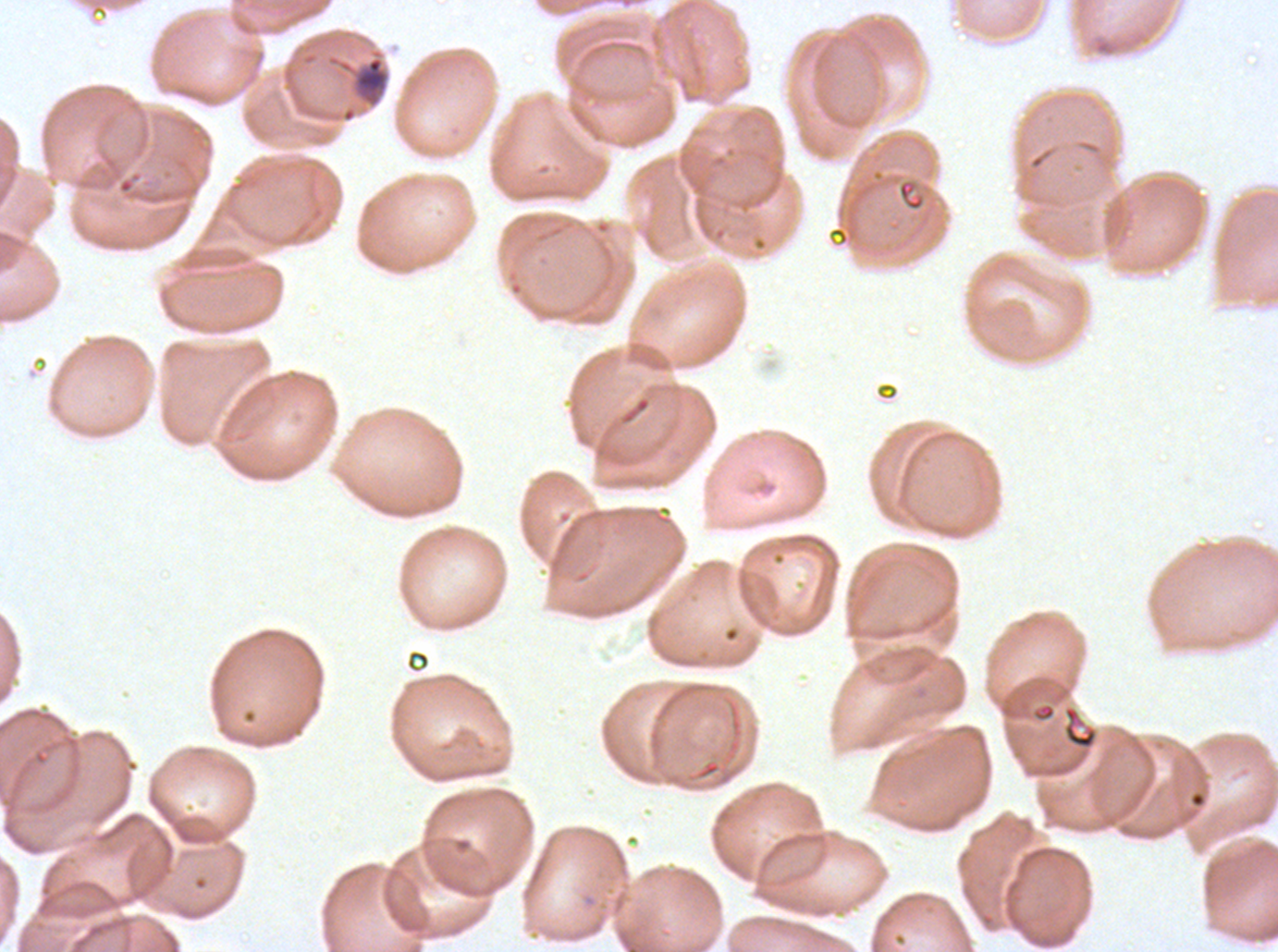

notation = approximate bounding boxes as (x1, y1, x2, y2) in pixels
mid trophozoite locations = (326, 47, 391, 109)
debris locations = (1062, 704, 1099, 751)
image size = 1278×952 pixels
specimen = ex-vivo Plasmodium falciparum culture from a patient in The Gambia, grown for 24 to 48 hours
preparation = thin blood film
field of view = one sub-image of a larger composite
stain = Giemsa